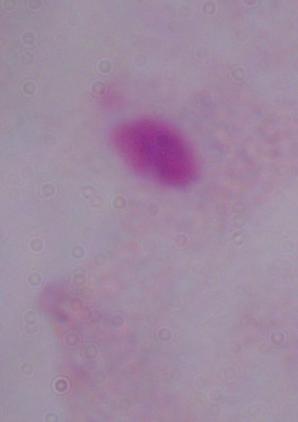
Summary:
  - Modality: micrograph
  - Identification: trichomonad
  - Magnification: 1000x